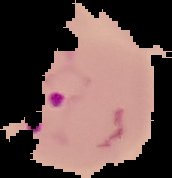 The area outside the segmented cell region is set to black. Malaria status: parasitized. Image is 172×178 pixels. From a thin blood smear.